Identify the preparation type.
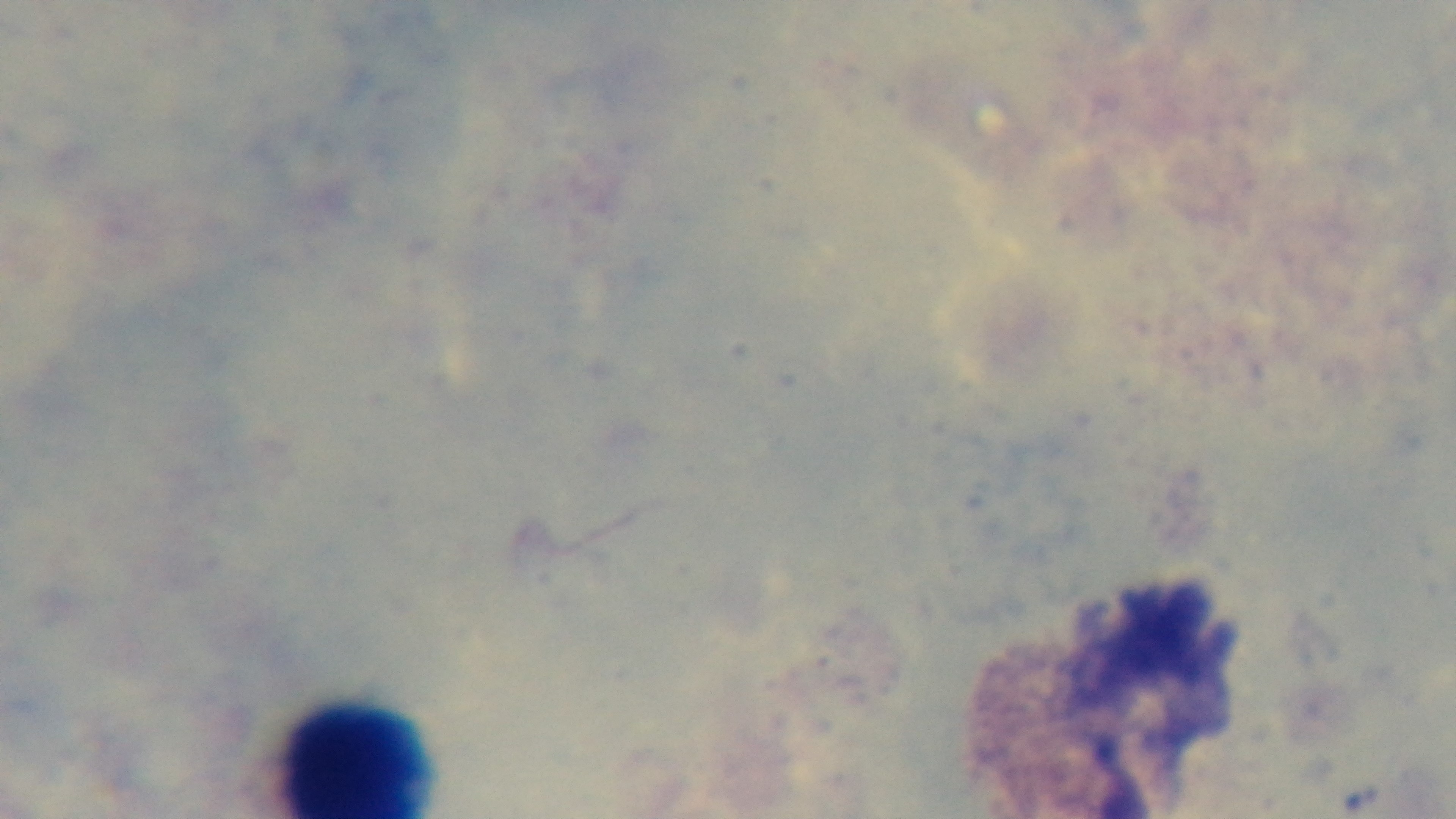

It is a thick blood film.

Summary:
  - Malaria status: uninfected
  - Objective: 100x oil immersion
  - Modality: light microscopy
  - Field of view: one from the slide
  - Capture: mounted 4K digital camera
  - Stain: Giemsa